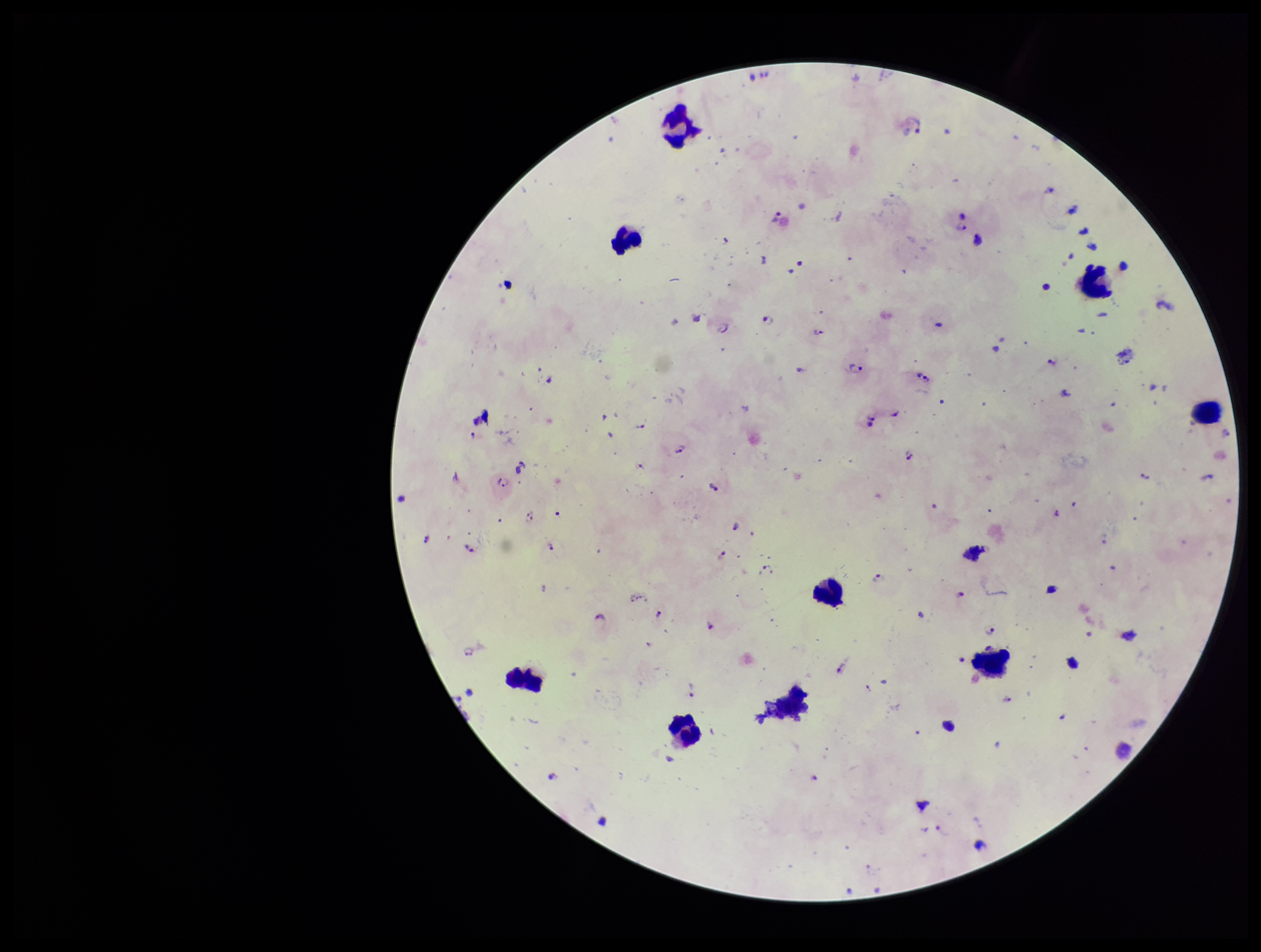

capture = smartphone photograph through the microscope eyepiece
field of view = single
image size = 1261×952 pixels
preparation = thick smear
species reported for this patient = Plasmodium falciparum
leukocyte count = 9
parasite count = 69
Plasmodium parasites = seen
patient malaria status = positive
stain = Giemsa